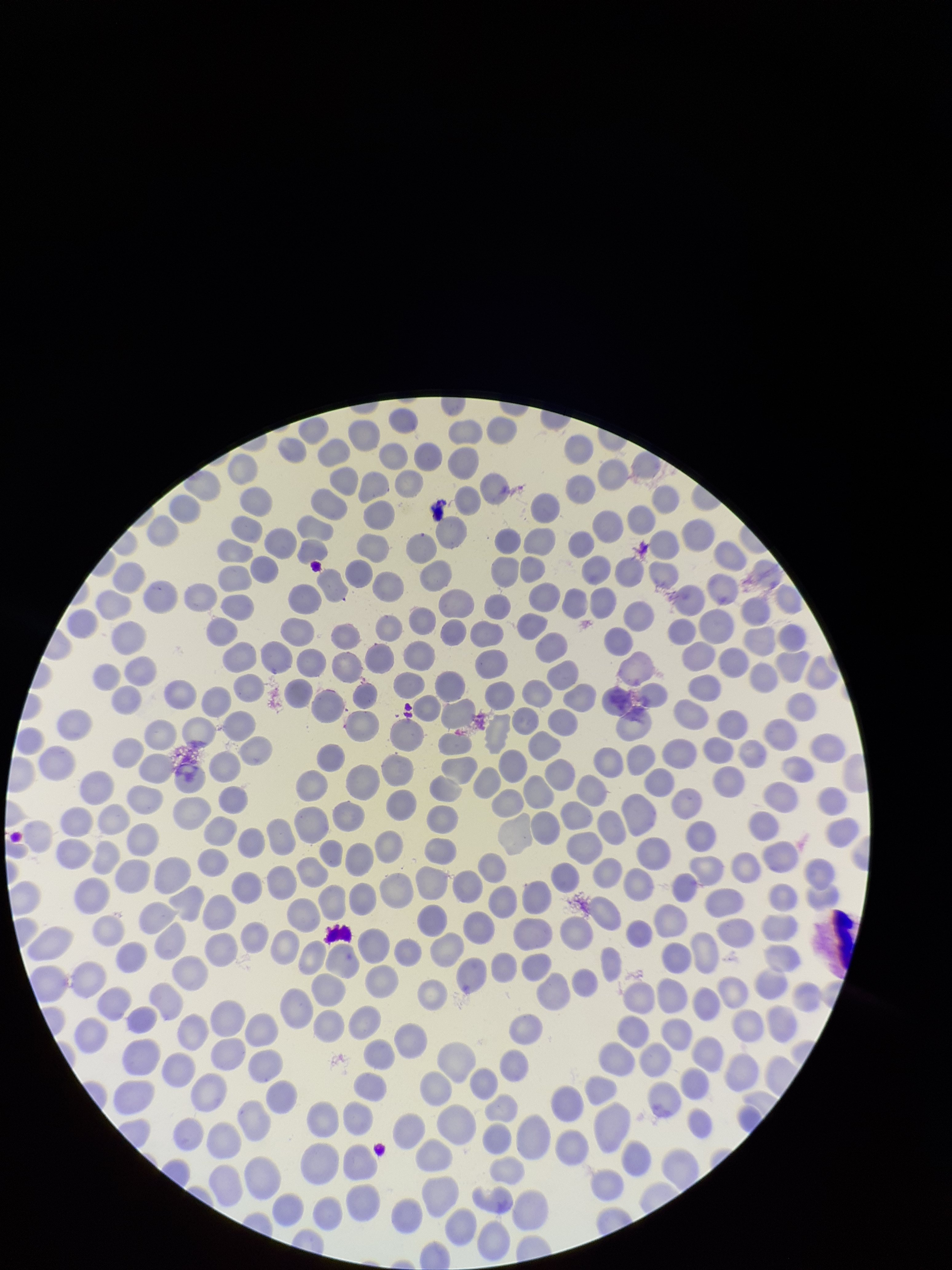
image size = 952×1270 pixels
preparation = thin blood smear
parasitized red blood cell count = 0
stain = Giemsa
parasitized red blood cells = none detected
red blood cell count = 340
patient malaria status = negative
capture = smartphone photograph through the microscope eyepiece
field of view = one from this slide